Identify the parasite.
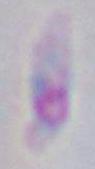
This is Toxoplasma gondii.

modality = micrograph
magnification = 1000x